Name the cell type shown.
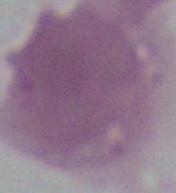

An erythrocyte.

Photomicrograph. Captured at 1000x magnification.